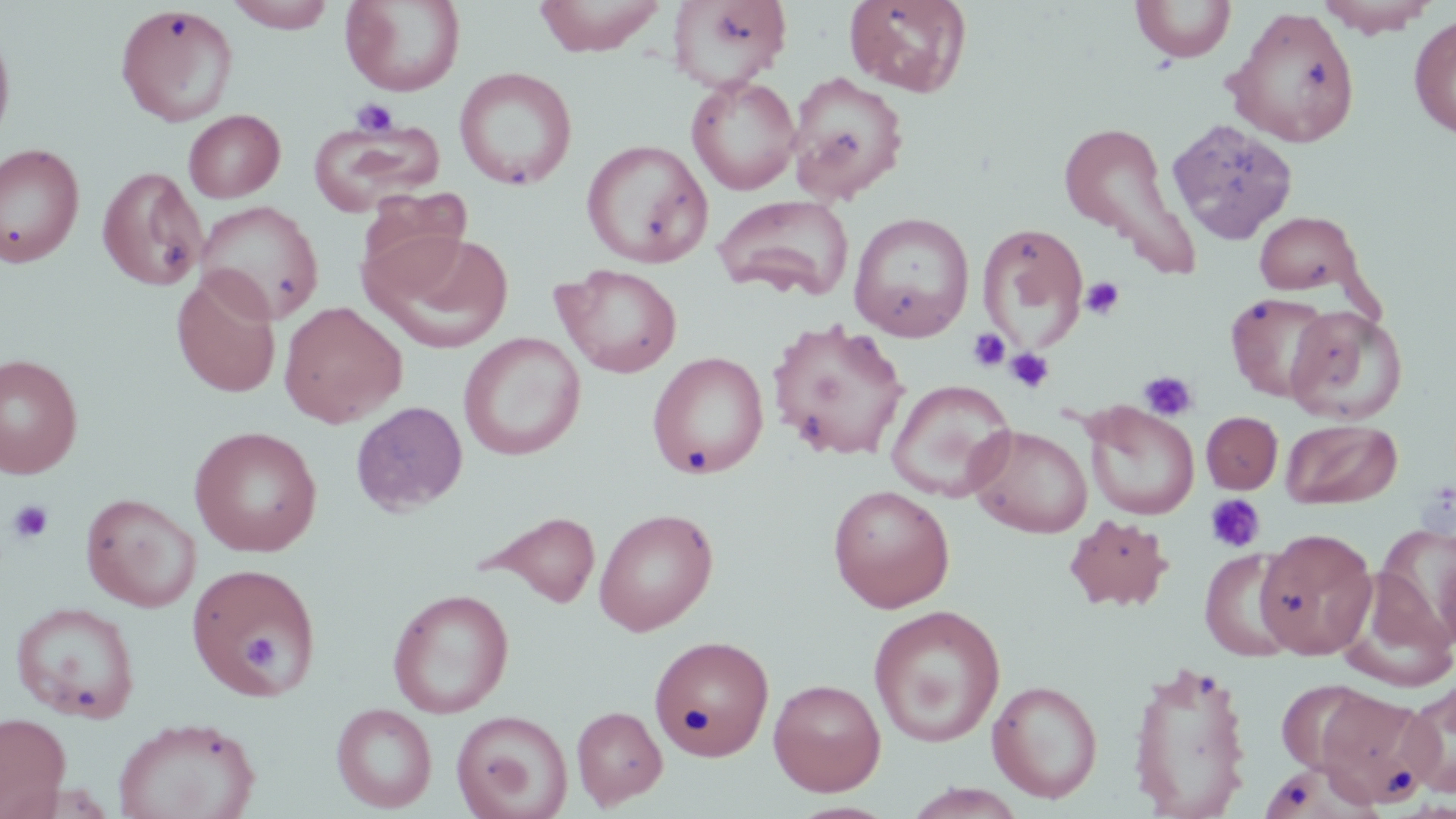

Summary:
  - Coordinate format: approximate bounding boxes as (x1, y1, x2, y2) in pixels
  - Uninfected red blood cell locations: (227, 0, 338, 32), (341, 0, 466, 96), (532, 0, 668, 56), (668, 0, 791, 91), (844, 0, 972, 97), (1131, 0, 1236, 62), (1316, 0, 1439, 37), (115, 5, 239, 126), (1224, 6, 1361, 147), (1409, 14, 1456, 139), (0, 20, 16, 151), (454, 67, 577, 190), (786, 71, 909, 204), (686, 74, 801, 195), (183, 109, 285, 202), (1166, 118, 1298, 244), (1057, 119, 1195, 267), (308, 120, 444, 216), (582, 139, 712, 268), (0, 143, 85, 267), (97, 166, 207, 291), (357, 187, 473, 298), (714, 193, 855, 302), (195, 199, 323, 323), (848, 211, 975, 341), (1254, 211, 1361, 295), (977, 222, 1088, 352), (370, 231, 515, 354), (556, 264, 682, 378), (171, 271, 281, 398), (1225, 291, 1331, 402), (279, 301, 407, 428), (1285, 305, 1408, 425), (767, 319, 911, 461), (459, 332, 585, 460), (647, 351, 769, 479), (0, 353, 83, 478), (885, 379, 1017, 501), (350, 401, 468, 516), (1081, 401, 1200, 520), (1202, 412, 1282, 494), (1281, 418, 1402, 509), (968, 424, 1093, 539), (189, 426, 322, 557), (828, 484, 955, 612), (80, 492, 201, 612), (593, 507, 719, 636), (477, 510, 601, 608), (1063, 514, 1175, 612), (1375, 525, 1456, 649), (1255, 529, 1377, 659), (1200, 549, 1300, 661), (186, 561, 322, 701), (1337, 570, 1456, 691), (387, 588, 515, 718), (9, 600, 141, 724), (869, 604, 1005, 748), (650, 635, 774, 760), (1126, 658, 1255, 817), (768, 678, 886, 796), (1402, 678, 1456, 798), (987, 679, 1103, 803), (1276, 679, 1380, 776), (1313, 687, 1438, 809), (331, 702, 438, 813), (571, 706, 667, 809), (452, 710, 573, 819), (0, 712, 71, 818), (111, 716, 261, 819), (1259, 761, 1380, 819), (902, 784, 1028, 819)
  - Platelet locations: (350, 98, 398, 137), (1080, 277, 1125, 321), (967, 328, 1011, 372), (1005, 348, 1054, 393), (1138, 370, 1197, 421), (1205, 493, 1266, 553), (7, 499, 54, 545), (243, 635, 281, 672)
  - Slide-level diagnosis: no evidence of blood parasites
  - Field of view: single
  - Modality: light microscopy
  - Magnification: 1000x
  - Preparation: thin blood smear
  - Image size: 1456×819 pixels
  - Stain: May-Grünwald-Giemsa